Report the malaria status of this cell.
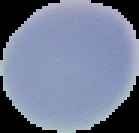

It is uninfected.

Summary:
  - Preparation: thin blood smear
  - Image size: 139×133 pixels
  - Image type: segmented cell region on a black background